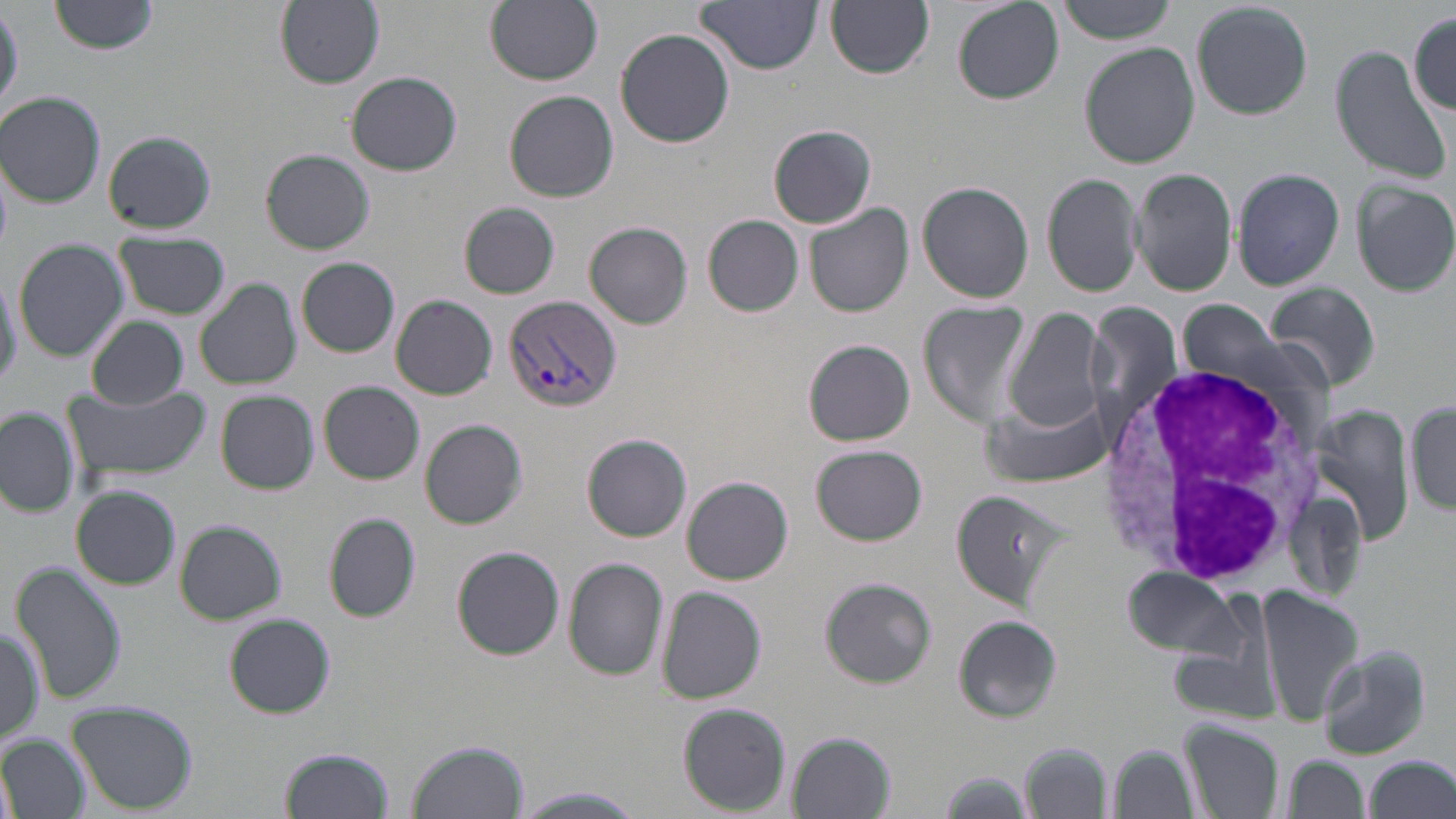

Approximate bounding boxes as [x1, y1, x2, y2] in pixels. Plasmodium vivax-infected red blood cell locations: [505, 295, 619, 415]. White blood cell locations: [1097, 364, 1331, 588]. Uninfected red blood cell locations: [49, 0, 161, 55], [274, 0, 385, 87], [486, 0, 605, 86], [825, 0, 935, 78], [1056, 0, 1177, 43], [695, 1, 824, 75], [952, 1, 1064, 106], [1189, 1, 1315, 121], [0, 4, 22, 119], [1409, 11, 1456, 117], [616, 29, 734, 148], [1080, 44, 1201, 168], [1329, 46, 1450, 185], [346, 71, 463, 176], [503, 90, 619, 203], [1, 91, 106, 207], [769, 125, 877, 228], [101, 131, 217, 233], [261, 148, 375, 254], [1230, 167, 1346, 290], [1131, 168, 1237, 296], [1041, 173, 1145, 298], [1350, 178, 1456, 296], [917, 181, 1034, 302], [806, 202, 915, 317], [460, 203, 560, 298], [703, 215, 804, 316], [586, 223, 691, 328], [115, 236, 232, 321], [11, 243, 130, 362], [297, 257, 400, 357], [0, 269, 22, 391], [194, 279, 302, 391], [1264, 281, 1383, 393], [389, 295, 498, 399], [1177, 298, 1301, 396], [920, 300, 1031, 424], [1088, 302, 1181, 425], [1002, 308, 1106, 433], [85, 316, 187, 409], [803, 339, 915, 446], [318, 381, 425, 485], [63, 383, 208, 482], [215, 390, 319, 494], [981, 393, 1116, 488], [1408, 401, 1455, 518], [1309, 405, 1416, 547], [0, 406, 77, 519], [419, 419, 528, 529], [583, 433, 691, 542], [812, 444, 927, 545], [680, 476, 794, 584], [72, 485, 181, 589], [948, 487, 1070, 608], [323, 511, 422, 624], [172, 519, 286, 625], [452, 545, 566, 659], [563, 558, 669, 680], [10, 561, 126, 707], [1121, 565, 1248, 658], [818, 576, 937, 688], [1253, 585, 1361, 729], [656, 586, 766, 704], [224, 614, 335, 718], [953, 615, 1063, 723], [1, 625, 46, 745], [1317, 643, 1434, 761], [67, 702, 200, 814], [678, 703, 790, 814], [1179, 720, 1283, 817], [788, 731, 894, 818], [2, 734, 86, 819], [408, 737, 530, 819], [1021, 740, 1113, 819], [1109, 743, 1196, 818], [279, 746, 396, 819], [1280, 756, 1369, 818], [1364, 756, 1454, 819], [938, 770, 1037, 818], [509, 787, 646, 819]. Slide-level diagnosis: Plasmodium vivax. May-Grünwald-Giemsa-stained preparation. Image is 1456×819 pixels. Thin blood smear. One field of a larger specimen. Light microscopy. Captured at 1000x magnification.